Classify this cell by malaria status.
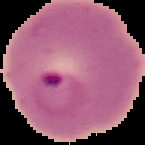
Parasitized.

preparation = thin blood smear
image size = 145×145 pixels
image type = segmented cell region on a black background